Locate every Plasmodium vivax-infected red blood cell.
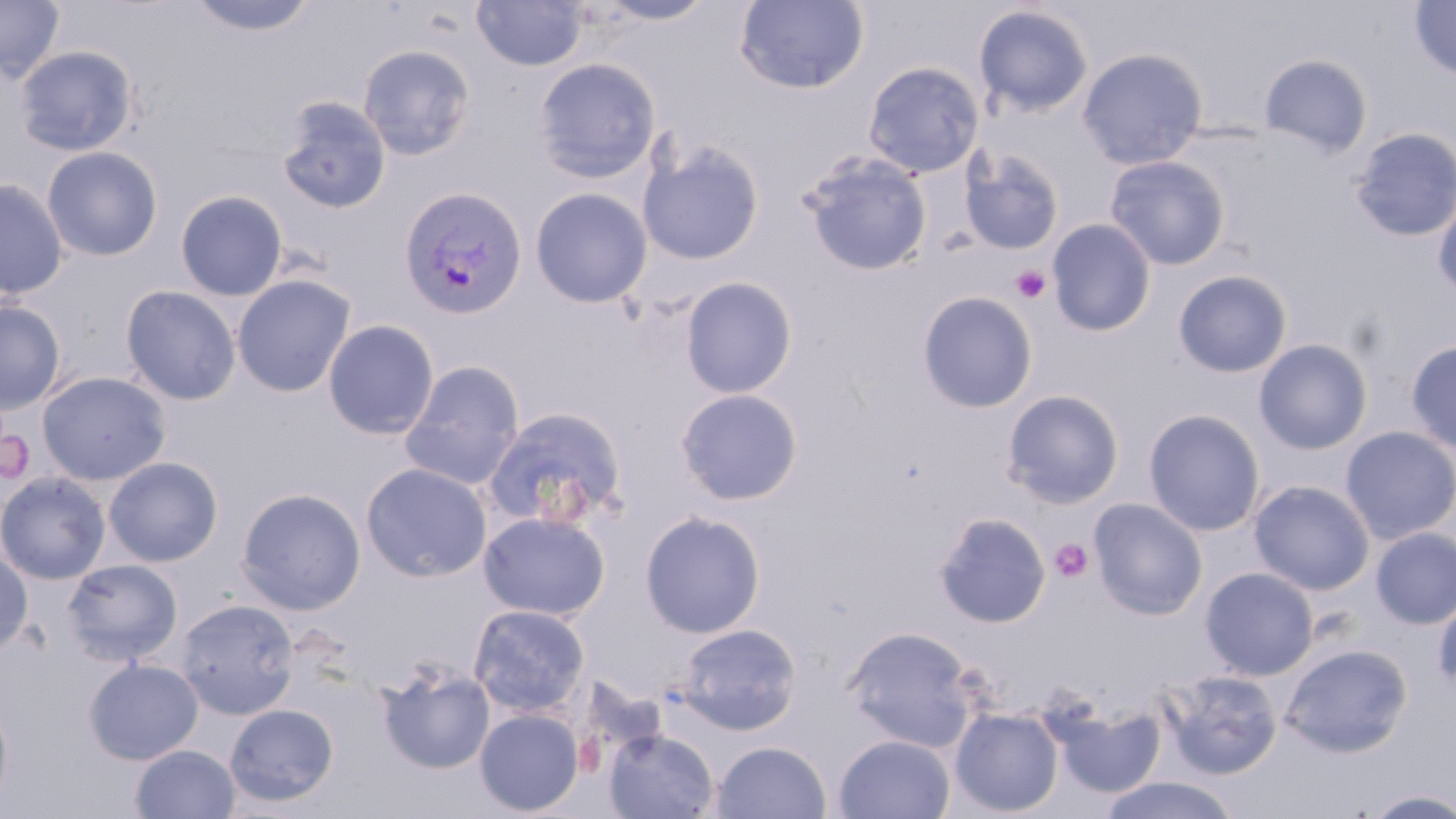
Approximate bounding boxes as (x1, y1, x2, y2) in pixels.
Plasmodium vivax-infected red blood cells: (398, 185, 529, 321).

Summary:
  - Platelet locations: (1011, 266, 1051, 303), (0, 426, 35, 486), (1049, 539, 1094, 584)
  - Uninfected red blood cell locations: (0, 0, 65, 83), (185, 0, 321, 38), (594, 0, 717, 27), (472, 1, 588, 71), (733, 1, 870, 94), (1409, 1, 1456, 80), (973, 5, 1094, 118), (358, 43, 476, 160), (14, 44, 139, 157), (1077, 47, 1209, 170), (1259, 53, 1373, 159), (532, 58, 661, 183), (862, 61, 984, 178), (275, 96, 392, 215), (1350, 126, 1456, 242), (638, 139, 765, 265), (41, 146, 164, 262), (959, 148, 1065, 255), (800, 152, 933, 276), (1104, 155, 1230, 270), (0, 177, 69, 300), (530, 187, 652, 308), (175, 190, 288, 301), (1433, 194, 1456, 303), (1047, 219, 1156, 337), (1173, 269, 1292, 378), (232, 274, 355, 397), (680, 277, 797, 399), (120, 285, 242, 405), (917, 291, 1038, 413), (0, 300, 66, 414), (322, 319, 439, 439), (1253, 338, 1373, 455), (1406, 339, 1456, 456), (400, 359, 526, 490), (37, 370, 172, 485), (675, 388, 804, 506), (1001, 389, 1125, 509), (482, 405, 630, 531), (1143, 408, 1266, 537), (1340, 426, 1456, 544), (103, 456, 223, 567), (360, 462, 493, 582), (0, 473, 110, 584), (1248, 480, 1375, 595), (236, 487, 366, 615), (1088, 497, 1209, 620), (639, 510, 766, 638), (478, 511, 611, 621), (932, 512, 1051, 629), (1371, 526, 1456, 629), (0, 551, 33, 656), (62, 558, 183, 666), (1200, 566, 1319, 680), (1433, 593, 1456, 698), (174, 598, 300, 719), (468, 603, 591, 718), (674, 622, 803, 735), (842, 625, 983, 752), (1281, 643, 1413, 757), (84, 658, 203, 765), (377, 661, 496, 775), (1161, 669, 1283, 779), (0, 695, 14, 813), (1047, 697, 1166, 801), (224, 704, 339, 807), (949, 706, 1064, 816), (474, 709, 584, 815), (604, 729, 719, 818), (833, 734, 956, 819), (711, 740, 832, 819), (130, 744, 240, 819), (1097, 776, 1242, 819), (1361, 789, 1456, 818)
  - Slide-level diagnosis: Plasmodium vivax
  - Image size: 1456×819 pixels
  - Magnification: 1000x
  - Field of view: single
  - Modality: light microscopy
  - Stain: May-Grünwald-Giemsa
  - Preparation: thin blood smear